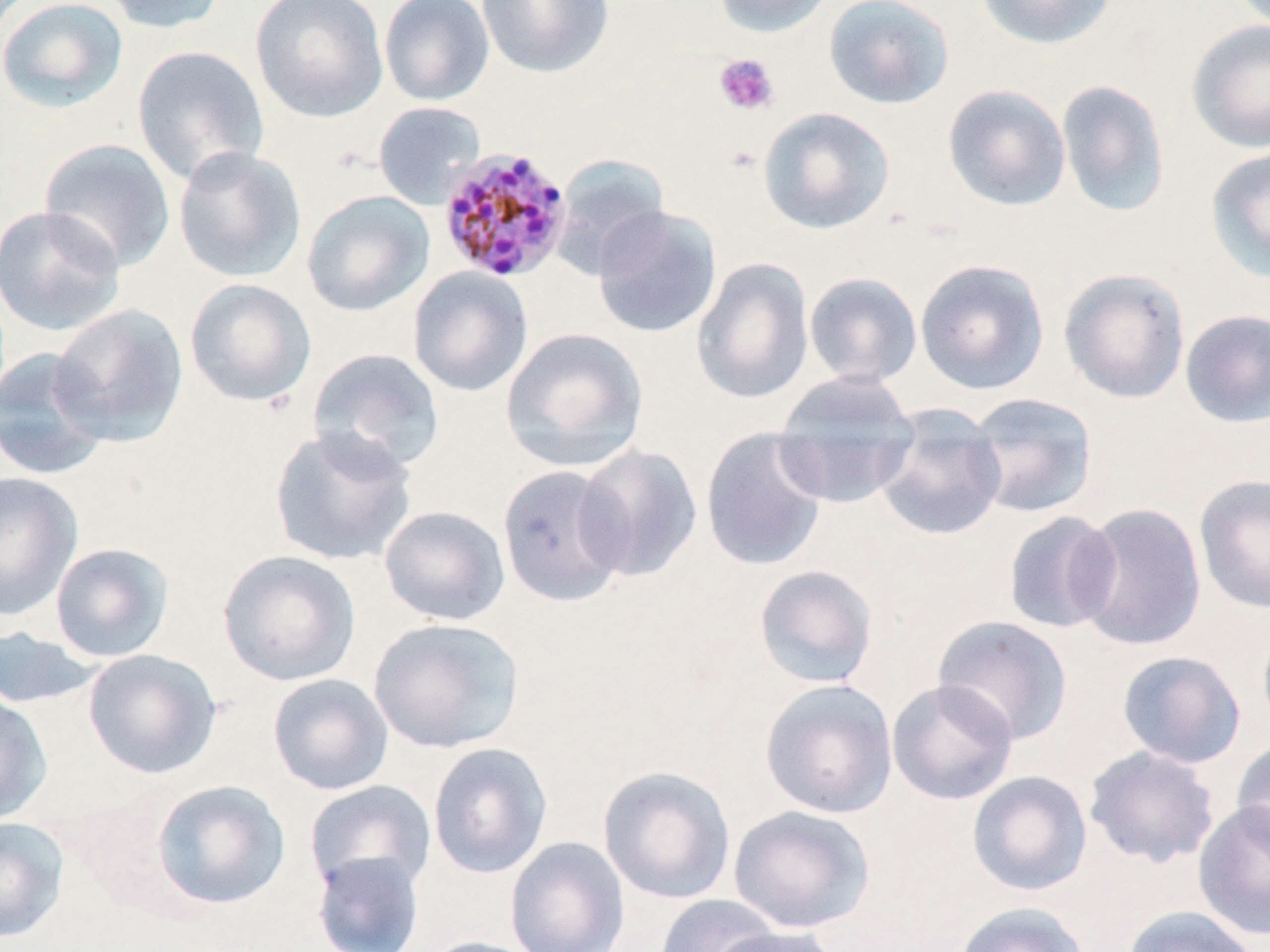 Approximate bounding boxes as [x1, y1, x2, y2] in pixels. Uninfected red blood cell locations: [0, 0, 129, 113], [100, 0, 230, 34], [250, 0, 389, 123], [379, 0, 494, 106], [476, 0, 614, 79], [711, 0, 837, 38], [824, 0, 955, 109], [975, 0, 1117, 50], [1186, 19, 1270, 153], [131, 45, 270, 187], [1056, 80, 1171, 218], [942, 84, 1071, 211], [373, 102, 486, 210], [758, 107, 895, 234], [39, 138, 177, 273], [173, 145, 307, 284], [1205, 146, 1270, 283], [549, 153, 672, 278], [301, 190, 435, 317], [0, 205, 127, 337], [591, 205, 722, 339], [691, 257, 815, 405], [915, 258, 1050, 395], [408, 267, 533, 397], [1058, 267, 1191, 404], [803, 272, 923, 387], [184, 278, 317, 408], [49, 303, 189, 446], [1179, 308, 1270, 427], [501, 327, 650, 473], [0, 346, 113, 481], [307, 347, 446, 476], [772, 370, 920, 509], [963, 392, 1098, 520], [873, 403, 1007, 542], [268, 425, 417, 567], [700, 426, 830, 572], [574, 443, 703, 582], [497, 464, 630, 607], [0, 471, 83, 621], [1193, 474, 1270, 613], [1073, 501, 1206, 651], [379, 505, 510, 626], [1002, 511, 1122, 634], [49, 541, 175, 663], [217, 550, 361, 686], [753, 564, 879, 689], [932, 615, 1074, 746], [368, 617, 526, 754], [1257, 618, 1270, 739], [0, 626, 98, 709], [82, 648, 222, 779], [1116, 651, 1247, 769], [267, 673, 394, 796], [886, 678, 1019, 805], [759, 679, 899, 819], [0, 692, 52, 825], [1232, 737, 1270, 859], [427, 742, 553, 879], [1084, 745, 1221, 868], [598, 765, 737, 904], [966, 770, 1092, 897], [149, 779, 292, 910], [304, 779, 436, 896], [1192, 799, 1270, 941], [728, 805, 875, 934], [0, 815, 70, 944], [505, 836, 630, 952], [311, 850, 426, 952], [654, 894, 783, 952], [952, 901, 1092, 952], [1121, 905, 1261, 952], [706, 924, 842, 952], [418, 935, 547, 952]. Plasmodium malariae-infected red blood cell locations: [437, 146, 574, 283]. Platelet locations: [713, 53, 779, 116]. Slide-level diagnosis: Plasmodium malariae. Thin blood film. Image is 1270×952 pixels. Light microscopy. Single field of view. May-Grünwald-Giemsa stain. Captured at 1000x magnification.